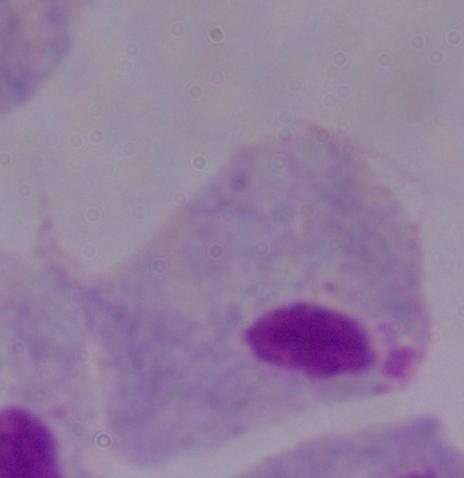
identification = trichomonad
modality = micrograph
magnification = 1000x